Report the malaria status of this cell.
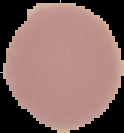

Uninfected.

From a thin blood film. Image is 124×133 pixels. Cell region segmented out of the field of view; the surrounding area is masked to black.